Name the blood parasite species.
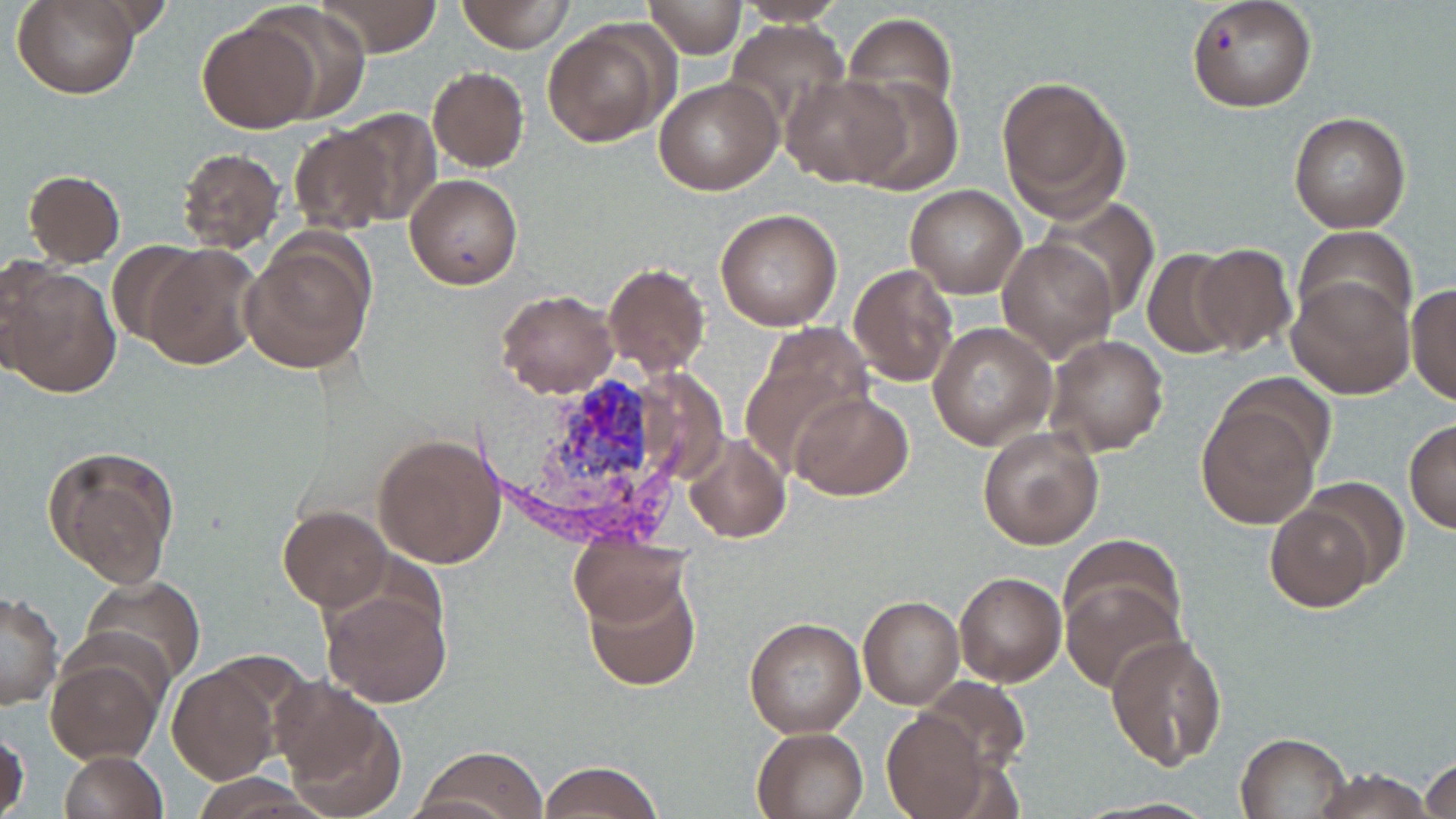

Plasmodium vivax.

Summary:
  - Coordinate format: approximate bounding boxes as [x1, y1, x2, y2] in pixels
  - Uninfected red blood cell locations: [15, 0, 138, 100], [316, 0, 444, 57], [457, 0, 574, 52], [730, 0, 856, 25], [1186, 0, 1315, 112], [642, 1, 747, 58], [250, 3, 374, 122], [844, 10, 957, 118], [541, 18, 672, 149], [197, 19, 319, 134], [723, 20, 852, 138], [427, 67, 529, 172], [779, 73, 911, 185], [996, 73, 1128, 219], [653, 74, 783, 195], [843, 76, 963, 195], [335, 108, 441, 223], [1288, 111, 1411, 233], [287, 127, 394, 236], [174, 147, 286, 255], [22, 169, 126, 267], [406, 174, 523, 291], [904, 184, 1026, 299], [1039, 198, 1160, 323], [714, 207, 842, 331], [1295, 227, 1417, 337], [997, 236, 1117, 362], [238, 238, 373, 375], [108, 239, 204, 347], [144, 244, 262, 371], [1191, 244, 1298, 356], [1142, 249, 1242, 358], [3, 262, 122, 399], [603, 263, 710, 376], [850, 263, 959, 387], [1288, 275, 1412, 399], [1406, 283, 1456, 404], [494, 287, 617, 399], [927, 322, 1057, 450], [740, 326, 873, 472], [1043, 335, 1167, 457], [1210, 374, 1336, 486], [791, 390, 913, 500], [1196, 406, 1320, 528], [1403, 419, 1456, 534], [978, 426, 1103, 550], [373, 432, 507, 568], [683, 432, 790, 543], [44, 445, 180, 587], [1299, 476, 1411, 591], [1265, 503, 1375, 613], [278, 506, 393, 611], [1058, 533, 1187, 645], [568, 535, 691, 629], [583, 568, 701, 691], [954, 571, 1067, 687], [78, 575, 206, 689], [1061, 578, 1183, 694], [319, 580, 454, 709], [1, 592, 63, 710], [858, 595, 964, 709], [744, 616, 866, 738], [1105, 632, 1228, 772], [46, 649, 167, 765], [168, 661, 283, 785], [918, 675, 1032, 776], [271, 678, 405, 815], [882, 709, 989, 816], [0, 721, 29, 819], [751, 726, 871, 819], [1235, 731, 1350, 817], [415, 747, 548, 817], [59, 750, 168, 819], [1419, 754, 1456, 817], [537, 760, 663, 819], [1309, 768, 1438, 818], [1083, 796, 1222, 816]
  - Plasmodium vivax-infected red blood cell locations: [534, 374, 660, 495]
  - Stain: May-Grünwald-Giemsa
  - Image size: 1456×819 pixels
  - Magnification: 1000x
  - Modality: light microscopy
  - Preparation: thin blood film
  - Field of view: one of a larger specimen